Point out each malaria parasite.
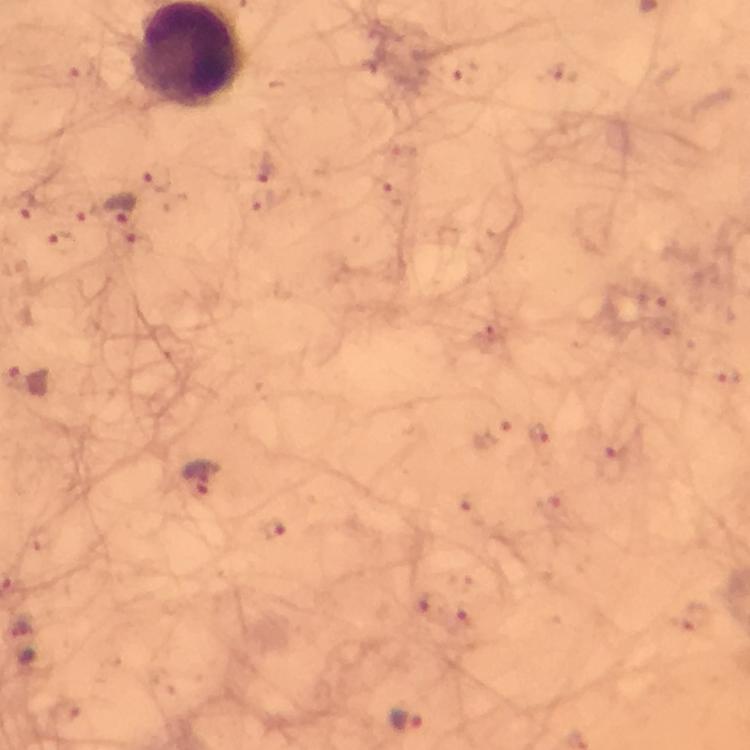
Approximate centers as (x, y) in pixels.
Malaria parasites: (464, 74), (558, 75), (265, 167), (155, 178), (394, 195), (262, 201), (24, 204), (116, 207), (59, 242), (138, 245), (652, 299), (492, 332), (725, 375), (494, 430), (538, 438), (611, 465), (203, 477), (553, 508), (472, 509), (272, 531), (429, 604), (467, 619), (698, 622), (64, 710), (405, 719).

Summary:
  - Image size: 750×750 pixels
  - Cropped from: one field of view
  - Capture: smartphone photograph through a microscope
  - Immersion oil: used
  - Context: from a diagnostic examination for malaria
  - Preparation: thick blood smear
  - Magnification: 100x
  - Stain: Giemsa